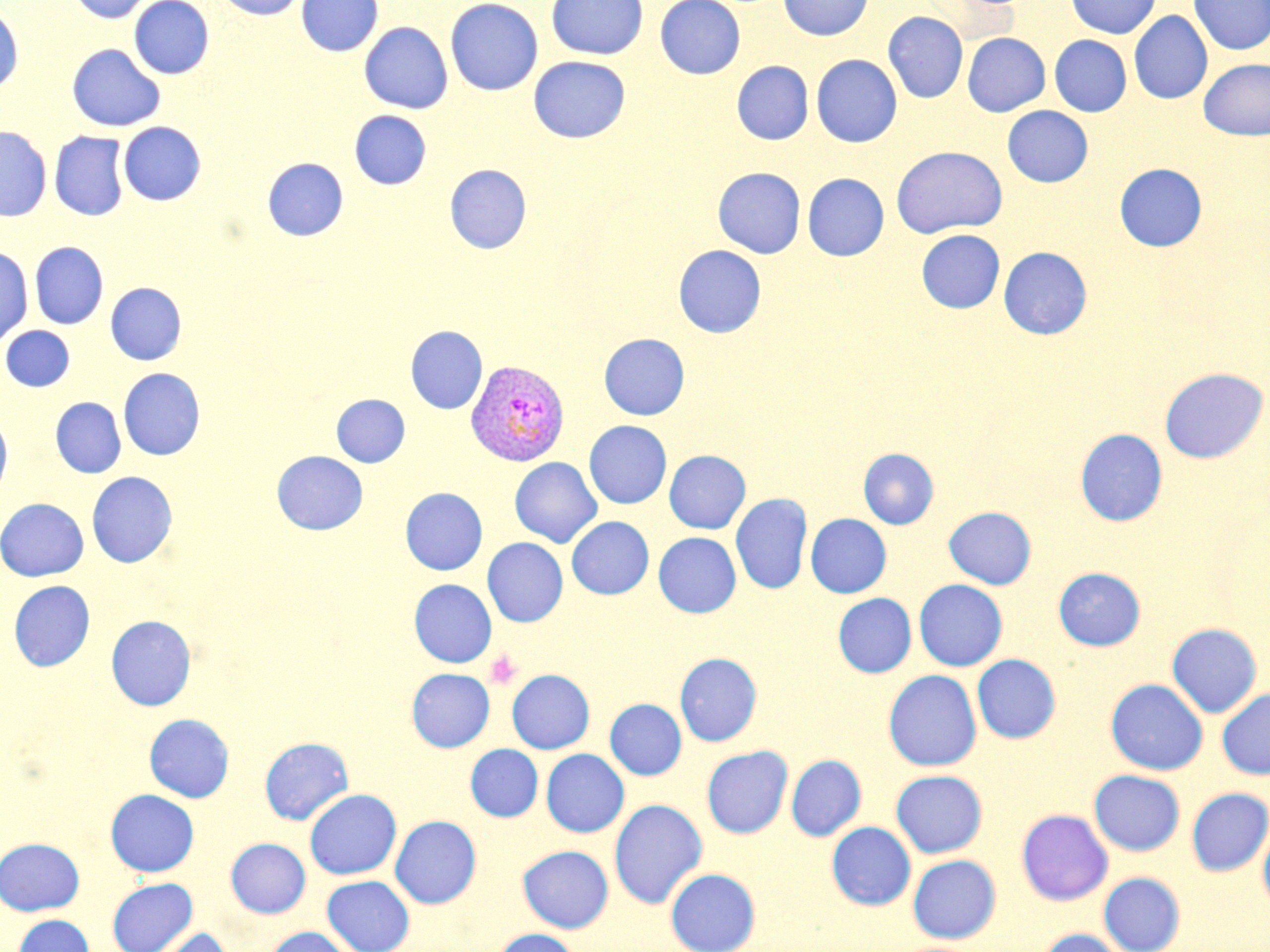 Approximate bounding boxes as [x1, y1, x2, y2] in pixels. Uninfected red blood cell locations: [69, 0, 155, 24], [129, 0, 214, 79], [215, 0, 307, 19], [296, 0, 383, 56], [445, 0, 544, 96], [546, 0, 648, 60], [655, 0, 745, 79], [778, 0, 873, 41], [1066, 0, 1160, 38], [1188, 0, 1270, 55], [0, 4, 24, 95], [1129, 11, 1212, 104], [883, 12, 968, 103], [359, 22, 453, 114], [962, 32, 1050, 117], [1049, 35, 1131, 117], [67, 43, 165, 131], [811, 54, 902, 147], [528, 56, 630, 144], [1198, 58, 1270, 140], [732, 61, 813, 144], [1003, 106, 1092, 187], [349, 110, 431, 190], [118, 121, 205, 205], [0, 126, 51, 221], [49, 132, 130, 220], [891, 146, 1007, 238], [263, 158, 348, 241], [1114, 163, 1207, 251], [444, 164, 531, 254], [713, 167, 805, 258], [803, 173, 889, 261], [916, 230, 1004, 313], [30, 242, 108, 329], [673, 245, 766, 337], [0, 246, 33, 347], [998, 247, 1092, 339], [106, 283, 187, 365], [1, 326, 74, 392], [406, 326, 487, 414], [599, 333, 690, 420], [1159, 367, 1268, 464], [118, 368, 205, 461], [331, 394, 410, 467], [51, 397, 126, 478], [0, 413, 12, 499], [584, 420, 671, 509], [1075, 428, 1167, 526], [858, 448, 939, 529], [664, 450, 750, 533], [272, 451, 368, 535], [510, 457, 602, 548], [87, 471, 177, 568], [400, 487, 487, 575], [731, 493, 812, 595], [0, 498, 88, 582], [943, 506, 1036, 589], [805, 514, 891, 597], [567, 516, 653, 599], [653, 532, 741, 618], [482, 538, 568, 627], [1053, 567, 1145, 650], [409, 579, 496, 667], [9, 580, 95, 671], [914, 580, 1007, 670], [833, 593, 916, 677], [106, 615, 196, 710], [1167, 623, 1262, 717], [674, 652, 762, 746], [972, 655, 1061, 743], [406, 668, 494, 751], [506, 669, 594, 754], [883, 669, 982, 771], [1106, 679, 1208, 775], [1217, 688, 1270, 779], [605, 698, 686, 779], [144, 713, 234, 802], [259, 737, 353, 825], [466, 744, 543, 821], [701, 746, 793, 838], [541, 749, 629, 837], [786, 754, 866, 840], [890, 770, 987, 857], [1089, 770, 1185, 856], [1186, 788, 1270, 875], [105, 789, 199, 876], [304, 789, 401, 879], [609, 799, 707, 908], [1016, 808, 1113, 905], [390, 815, 481, 908], [1258, 821, 1270, 915], [827, 822, 916, 910], [0, 837, 85, 915], [226, 838, 310, 917], [518, 845, 613, 932], [908, 854, 1001, 943], [666, 868, 760, 952], [1099, 872, 1185, 952], [322, 875, 414, 952], [107, 877, 197, 951], [13, 914, 94, 952], [263, 926, 354, 952], [140, 927, 232, 952], [492, 928, 581, 952], [1036, 928, 1128, 952]. Plasmodium vivax-infected red blood cell locations: [466, 359, 569, 466]. Platelet locations: [485, 650, 522, 690]. Slide-level diagnosis: Plasmodium vivax. Light microscopy. Thin blood smear. May-Grünwald-Giemsa-stained preparation. Single field of view. 1000x magnification. Image is 1270×952 pixels.